State which parasite is depicted.
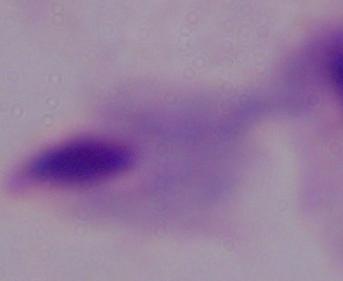

A trichomonad.

magnification = 1000x
modality = micrograph